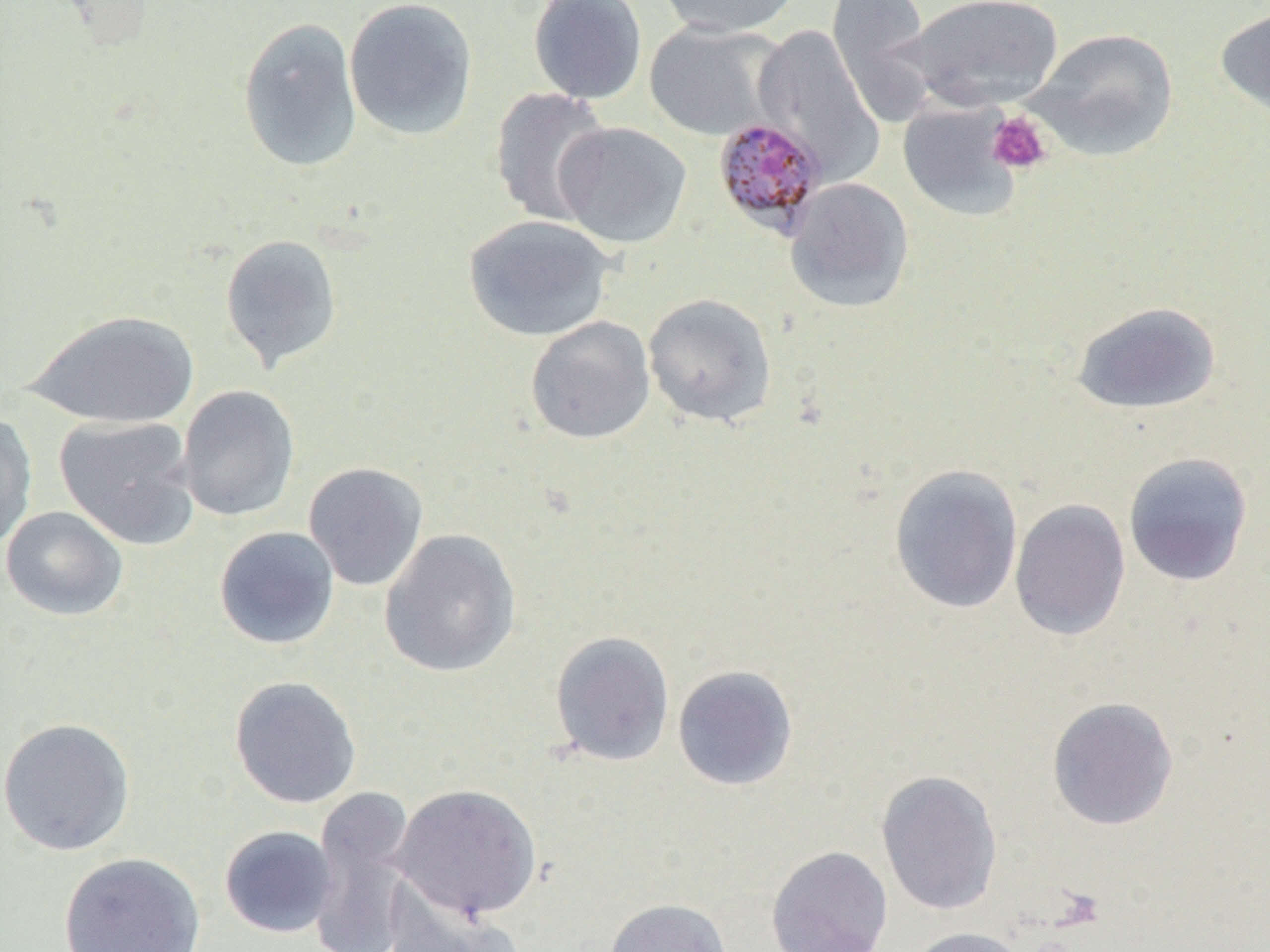
Summary:
  - Coordinate format: approximate bounding boxes as [x1, y1, x2, y2] in pixels
  - Uninfected red blood cell locations (subset): [344, 0, 479, 141], [528, 0, 648, 106], [654, 0, 804, 38], [827, 0, 940, 127], [904, 0, 1064, 113], [1214, 6, 1270, 123], [237, 16, 363, 172], [643, 20, 785, 142], [752, 23, 885, 184], [1029, 27, 1180, 160], [489, 87, 612, 227], [553, 121, 692, 249], [784, 177, 915, 313], [462, 214, 616, 342], [219, 233, 343, 372], [642, 292, 778, 427], [1070, 301, 1223, 415], [23, 310, 201, 428], [525, 316, 656, 444], [176, 385, 300, 522], [0, 412, 37, 550], [54, 415, 200, 549], [1122, 451, 1254, 586], [302, 462, 429, 591], [889, 463, 1024, 614], [1009, 498, 1131, 641], [1, 506, 129, 621], [213, 526, 340, 650], [379, 528, 522, 678], [550, 630, 675, 767], [672, 664, 798, 791], [229, 675, 362, 809], [1046, 696, 1180, 831], [0, 717, 136, 857], [875, 768, 1003, 916], [392, 783, 542, 921], [307, 788, 416, 952], [219, 825, 337, 938], [766, 845, 893, 952], [58, 851, 206, 952], [384, 885, 524, 952], [604, 898, 732, 952], [904, 926, 1031, 952]
  - Platelet locations (subset): [986, 110, 1052, 175]
  - Slide-level diagnosis: Plasmodium malariae
  - Image size: 1270×952 pixels
  - Magnification: 1000x
  - Field of view: single
  - Preparation: thin blood smear
  - Modality: optical microscopy